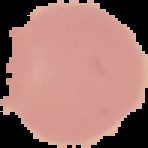
Summary:
  - Image type: segmented cell region on a black background
  - Preparation: thin blood film
  - Malaria status: uninfected
  - Image size: 148×148 pixels